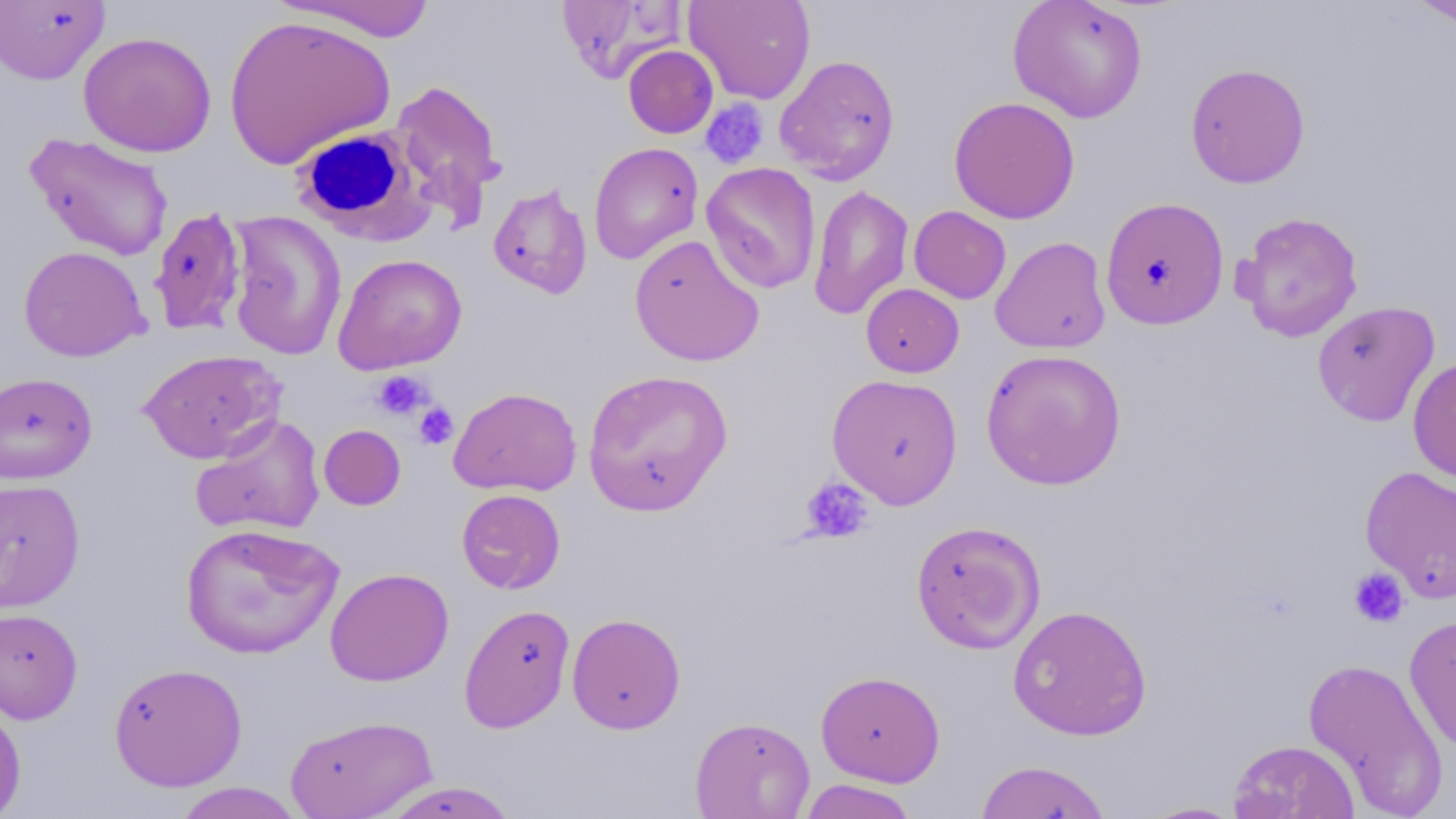

{
  "slide_level_diagnosis": "no evidence of blood parasites",
  "uninfected_red_blood_cell_locations": "approximate bounding boxes as (x1,y1)-(x2,y2) corner pairs in pixels: (555,0)-(689,84), (684,0)-(816,105), (1008,0)-(1148,123), (1405,0)-(1456,27), (0,1)-(110,85), (271,1)-(439,42), (221,14)-(395,169), (78,31)-(217,158), (622,42)-(717,136), (775,55)-(900,184), (1185,63)-(1311,188), (389,79)-(506,216), (949,96)-(1080,224), (24,132)-(174,261), (588,142)-(703,264), (701,162)-(822,294), (488,183)-(593,299), (808,184)-(913,321), (1101,196)-(1229,329), (149,206)-(248,336), (909,206)-(1011,304), (225,211)-(347,360), (1233,211)-(1365,342), (629,234)-(764,366), (991,236)-(1111,354), (18,245)-(149,362), (332,253)-(467,374), (861,284)-(964,377), (1312,300)-(1440,426), (138,349)-(283,463), (980,349)-(1127,490), (1408,356)-(1456,486), (582,368)-(733,515), (0,372)-(98,484), (826,373)-(964,508), (449,387)-(582,496), (190,415)-(326,537), (318,424)-(406,510), (1360,466)-(1456,603), (0,478)-(85,612), (456,489)-(565,594), (911,520)-(1046,654), (180,522)-(343,660), (325,568)-(454,687), (458,603)-(575,733), (1008,604)-(1152,740), (0,607)-(83,724), (567,612)-(686,734), (1404,614)-(1456,753), (1303,657)-(1449,816), (108,662)-(247,791), (816,669)-(945,787), (0,699)-(26,819), (284,714)-(436,819), (689,716)-(815,818), (1229,739)-(1359,818), (974,760)-(1112,819), (797,779)-(919,819), (376,781)-(521,818), (172,782)-(306,818), (1137,801)-(1246,818)",
  "modality": "optical microscopy",
  "stain": "May-Grünwald-Giemsa",
  "field_of_view": "single",
  "image_size": "1456×819 pixels",
  "preparation": "thin blood smear",
  "magnification": "1000x",
  "platelet_locations": "approximate bounding boxes as (x1,y1)-(x2,y2) corner pairs in pixels: (704,100)-(773,171), (371,370)-(432,421), (413,402)-(458,449), (800,476)-(873,544), (1348,567)-(1409,628)",
  "white_blood_cell_locations": "approximate bounding boxes as (x1,y1)-(x2,y2) corner pairs in pixels: (291,125)-(433,244)"
}